Give the extent of all uninfected red blood cells.
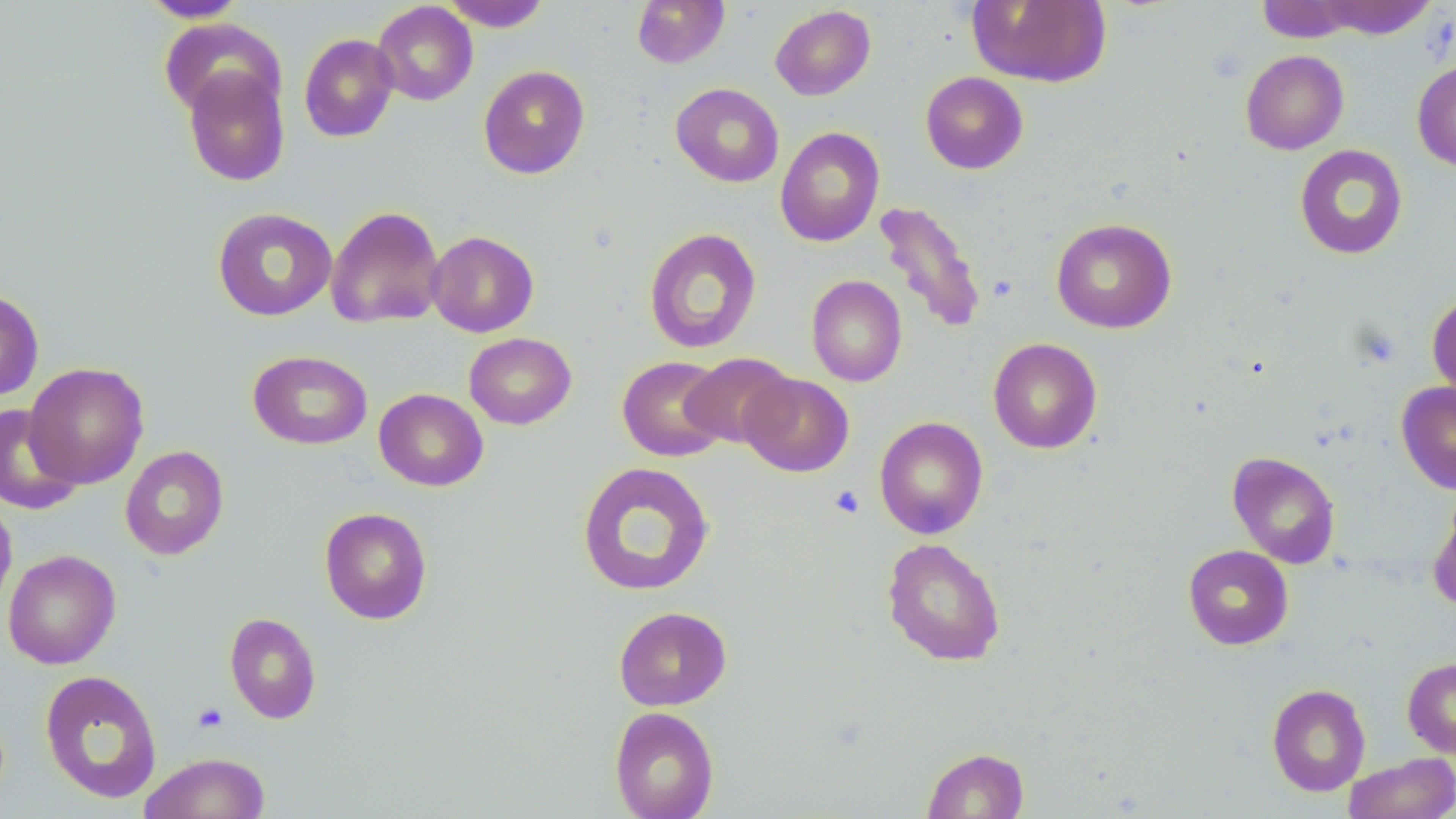

Approximate bounding boxes as [x1, y1, x2, y2] in pixels.
Uninfected red blood cells: [139, 0, 251, 22], [441, 0, 552, 31], [632, 0, 730, 68], [967, 0, 1113, 88], [1306, 0, 1439, 40], [1257, 1, 1363, 42], [372, 2, 478, 106], [770, 5, 876, 101], [159, 18, 284, 120], [298, 33, 399, 142], [1240, 50, 1349, 155], [1412, 59, 1456, 172], [478, 65, 590, 179], [182, 66, 291, 187], [920, 71, 1029, 174], [671, 83, 784, 188], [775, 126, 885, 247], [1294, 144, 1408, 259], [873, 200, 987, 335], [325, 205, 445, 329], [212, 207, 337, 321], [1050, 217, 1177, 334], [644, 227, 762, 354], [427, 230, 539, 337], [806, 275, 907, 387], [0, 289, 44, 401], [1427, 293, 1456, 401], [464, 332, 577, 430], [988, 338, 1102, 453], [248, 349, 372, 450], [681, 352, 796, 449], [617, 356, 730, 461], [23, 362, 149, 489], [739, 373, 854, 477], [1396, 381, 1456, 494], [374, 388, 489, 491], [0, 403, 84, 515], [874, 415, 988, 539], [120, 445, 229, 560], [1227, 451, 1341, 568], [576, 461, 715, 596], [1429, 488, 1456, 612], [0, 496, 17, 618], [319, 506, 433, 624], [882, 537, 1006, 666], [1183, 544, 1293, 650], [3, 549, 121, 670], [613, 606, 731, 711], [224, 613, 322, 724], [1402, 656, 1456, 759], [39, 669, 162, 804], [1266, 683, 1371, 796], [609, 706, 720, 819], [922, 747, 1029, 818], [138, 752, 270, 818], [1343, 753, 1456, 819].

Platelet locations: [828, 485, 865, 518], [192, 703, 229, 732]. Slide-level diagnosis: negative for blood parasites. Captured at 1000x magnification. Single field of view. Thin blood smear. May-Grünwald-Giemsa-stained preparation. Optical microscopy. Image is 1456×819 pixels.